Name the parasite shown.
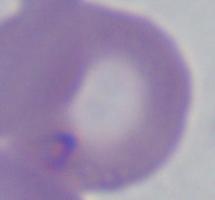

Babesia.

modality = micrograph
magnification = 1000x